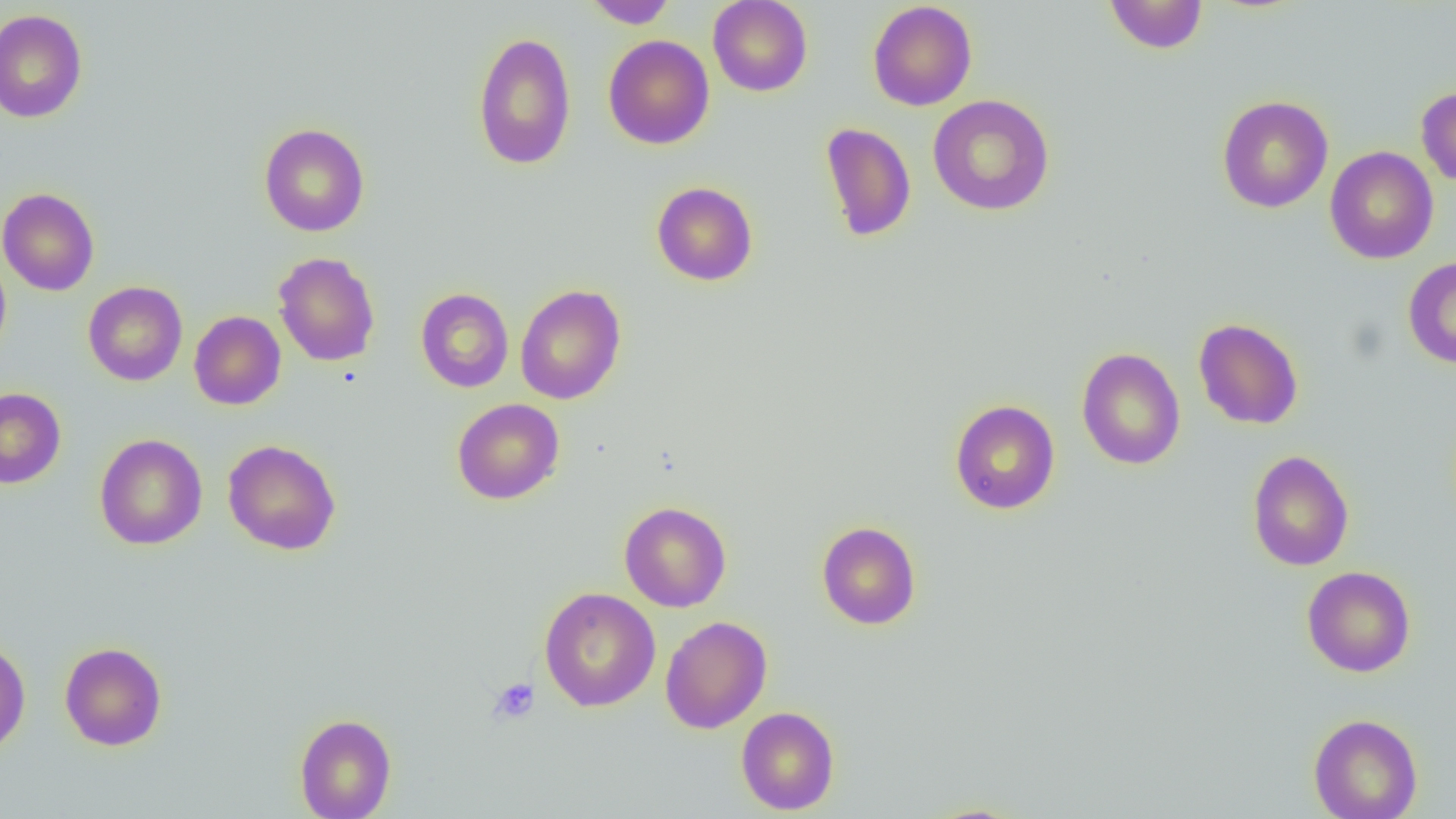
Summary:
  - Coordinate format: approximate bounding boxes as (x1, y1, x2, y2) in pixels
  - Uninfected red blood cell locations: (583, 0, 677, 29), (708, 0, 812, 97), (1103, 0, 1209, 54), (867, 1, 977, 111), (0, 9, 88, 123), (472, 31, 576, 171), (603, 35, 715, 150), (1416, 86, 1456, 187), (927, 94, 1055, 216), (1216, 95, 1333, 213), (819, 122, 916, 242), (258, 123, 370, 237), (1324, 146, 1439, 264), (651, 181, 758, 286), (0, 187, 100, 296), (0, 249, 12, 363), (273, 252, 380, 366), (1402, 255, 1456, 369), (83, 281, 187, 386), (515, 284, 627, 405), (415, 287, 514, 393), (189, 310, 286, 410), (1193, 318, 1304, 430), (1077, 347, 1186, 470), (0, 387, 66, 488), (451, 398, 565, 505), (949, 399, 1060, 514), (94, 433, 208, 550), (222, 439, 341, 555), (1247, 450, 1355, 571), (619, 501, 732, 612), (816, 521, 921, 630), (1302, 565, 1416, 678), (539, 587, 660, 711), (660, 616, 773, 734), (0, 638, 31, 756), (59, 642, 167, 751), (736, 706, 840, 815), (294, 713, 396, 819), (1308, 713, 1423, 819), (918, 802, 1032, 818)
  - Platelet locations: (488, 677, 540, 724)
  - Slide-level diagnosis: no evidence of blood parasites
  - Preparation: thin blood film
  - Modality: optical microscopy
  - Field of view: one of a larger specimen
  - Magnification: 1000x
  - Image size: 1456×819 pixels